Outline each Plasmodium vivax-infected red blood cell.
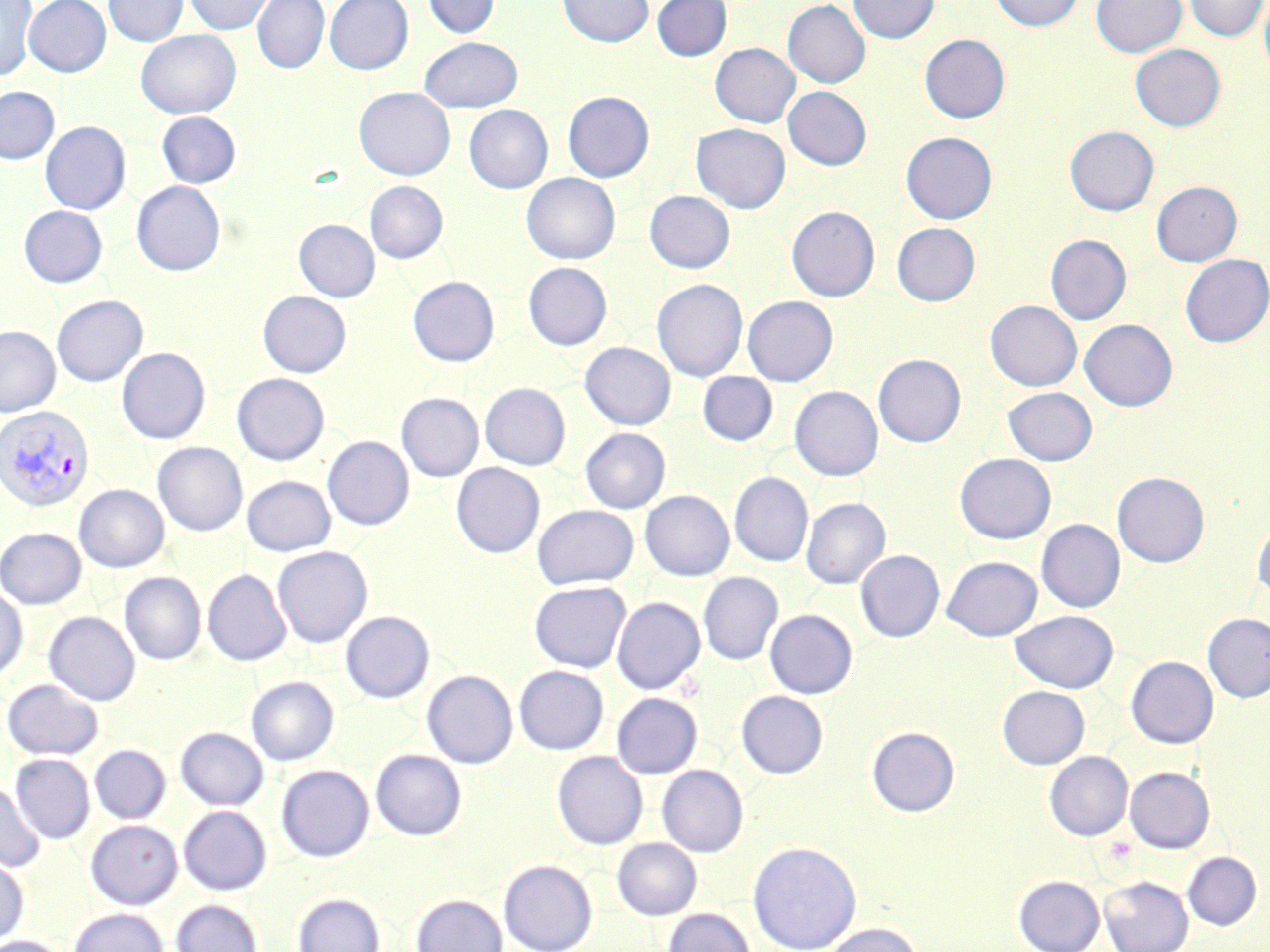
Approximate bounding boxes as (x1,y1)-(x2,y2) corner pairs in pixels.
Plasmodium vivax-infected red blood cells: (0,405)-(95,512).

{
  "slide_level_diagnosis": "Plasmodium vivax",
  "preparation": "thin blood smear",
  "field_of_view": "single",
  "stain": "May-Grünwald-Giemsa",
  "uninfected_red_blood_cell_locations": "approximate bounding boxes as (x1,y1)-(x2,y2) corner pairs in pixels: (0,0)-(37,81), (24,0)-(111,78), (103,0)-(189,47), (184,0)-(275,35), (252,0)-(330,74), (325,0)-(413,75), (422,0)-(500,39), (557,0)-(654,47), (652,0)-(732,61), (847,0)-(939,44), (990,0)-(1083,31), (1091,0)-(1186,57), (1183,0)-(1268,41), (1259,0)-(1270,80), (783,1)-(870,88), (135,30)-(241,119), (919,34)-(1010,124), (419,37)-(523,112), (710,43)-(800,128), (1130,43)-(1226,131), (0,86)-(59,164), (354,87)-(455,181), (783,87)-(872,171), (562,91)-(654,182), (463,105)-(553,194), (156,111)-(242,189), (40,121)-(131,215), (691,123)-(790,213), (1064,125)-(1159,216), (900,132)-(997,224), (521,173)-(620,265), (131,181)-(226,276), (365,181)-(448,264), (1151,181)-(1242,267), (645,191)-(735,274), (18,205)-(108,288), (787,206)-(880,302), (294,219)-(379,302), (892,222)-(980,306), (1045,234)-(1131,324), (1180,254)-(1270,347), (523,262)-(612,350), (407,276)-(499,367), (652,279)-(748,381), (258,291)-(351,377), (52,295)-(148,387), (742,296)-(838,386), (985,300)-(1082,391), (1080,319)-(1178,411), (0,325)-(60,417), (580,342)-(676,431), (116,347)-(210,444), (873,354)-(966,447), (697,371)-(778,446), (232,374)-(330,465), (480,383)-(571,470), (790,386)-(883,481), (1003,387)-(1098,465), (397,393)-(483,482), (580,428)-(671,514), (323,436)-(414,531), (152,442)-(247,536), (955,453)-(1056,544), (451,462)-(545,559), (1112,472)-(1210,567), (729,473)-(813,567), (242,476)-(336,557), (74,484)-(169,573), (640,490)-(733,581), (801,497)-(890,589), (532,505)-(638,590), (1251,517)-(1270,599), (1036,519)-(1125,613), (0,527)-(86,610), (272,546)-(372,648), (855,550)-(945,642), (942,555)-(1043,642), (203,569)-(291,667), (120,572)-(206,665), (698,572)-(783,665), (529,581)-(631,673), (0,585)-(28,683), (612,597)-(705,694), (765,609)-(858,699), (1009,610)-(1119,693), (340,611)-(434,703), (44,612)-(140,706), (1202,612)-(1270,703), (1125,656)-(1219,748), (514,666)-(609,755), (422,670)-(518,769), (246,676)-(339,766), (2,679)-(104,761), (997,685)-(1090,769), (736,690)-(828,779), (611,692)-(702,779), (867,726)-(960,817), (175,727)-(268,810), (89,745)-(171,824), (370,749)-(467,841), (552,751)-(648,850), (1044,751)-(1133,841), (10,754)-(95,844), (657,764)-(748,857), (276,765)-(374,862), (1125,766)-(1215,853), (0,781)-(45,873), (179,805)-(272,895), (85,820)-(183,909), (612,837)-(702,920), (747,840)-(862,952), (1182,852)-(1261,931), (0,854)-(29,946), (499,859)-(598,952), (1013,875)-(1105,952), (1099,876)-(1193,952), (292,892)-(385,952), (411,894)-(507,952), (171,899)-(262,952), (661,907)-(756,952), (68,908)-(168,952), (820,922)-(924,952), (1,935)-(69,952)",
  "magnification": "1000x",
  "modality": "optical microscopy",
  "image_size": "1270×952 pixels"
}